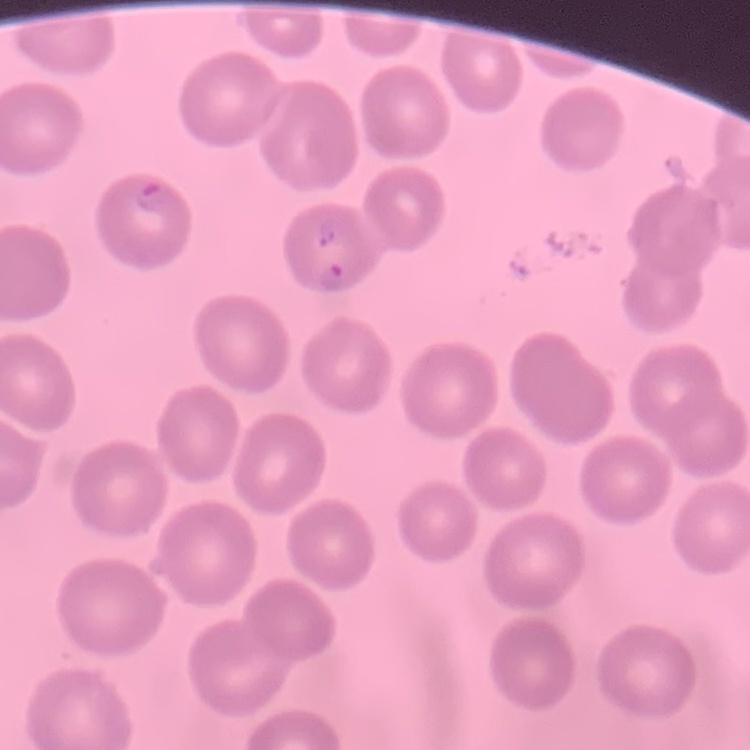

The red blood cells exhibit no rouleaux formation. One tile cut from a larger photomicrograph. Stained with either Field's or Giemsa. Thin blood smear.